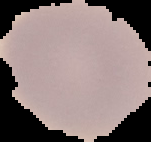

Summary:
  - Malaria status: uninfected
  - Image type: cell region segmented out of the field of view; surrounding area masked to black
  - Preparation: thin blood smear
  - Image size: 151×142 pixels